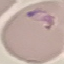 Result: malaria parasites identified. Acquired by smartphone through the microscope eyepiece. Automatically extracted cell patch, resized to 64 × 64 pixels. Thin blood film. Giemsa-stained preparation.